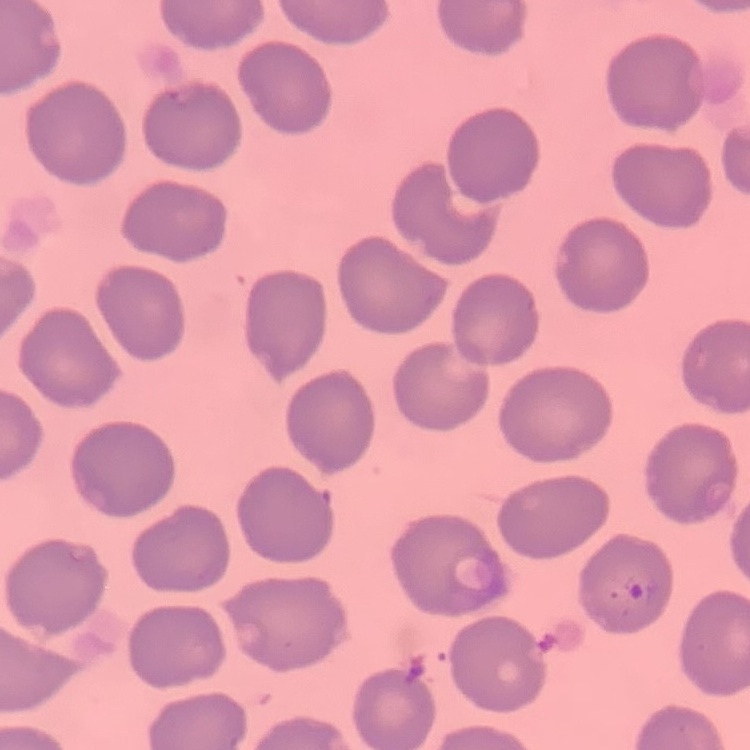
The red blood cells exhibit no rouleaux formation. Square crop of a larger photomicrograph. Thin peripheral smear. Field's or Giemsa stain.